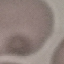
Result: no malaria parasites seen. Automatically extracted cell patch, resized to 64 × 64 pixels. Photographed with a smartphone camera at the microscope eyepiece. Giemsa stain. Thin blood film.